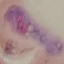

Summary:
  - Result: malaria parasites identified
  - Stain: Giemsa
  - Capture: smartphone through the microscope eyepiece
  - Preparation: thin smear
  - Image type: automatically extracted cell patch, resized to 64 × 64 pixels